Classify this cell by malaria status.
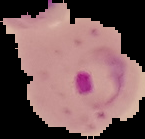

Parasitized.

image size = 145×139 pixels
image type = segmented cell region on a black background
preparation = thin blood smear